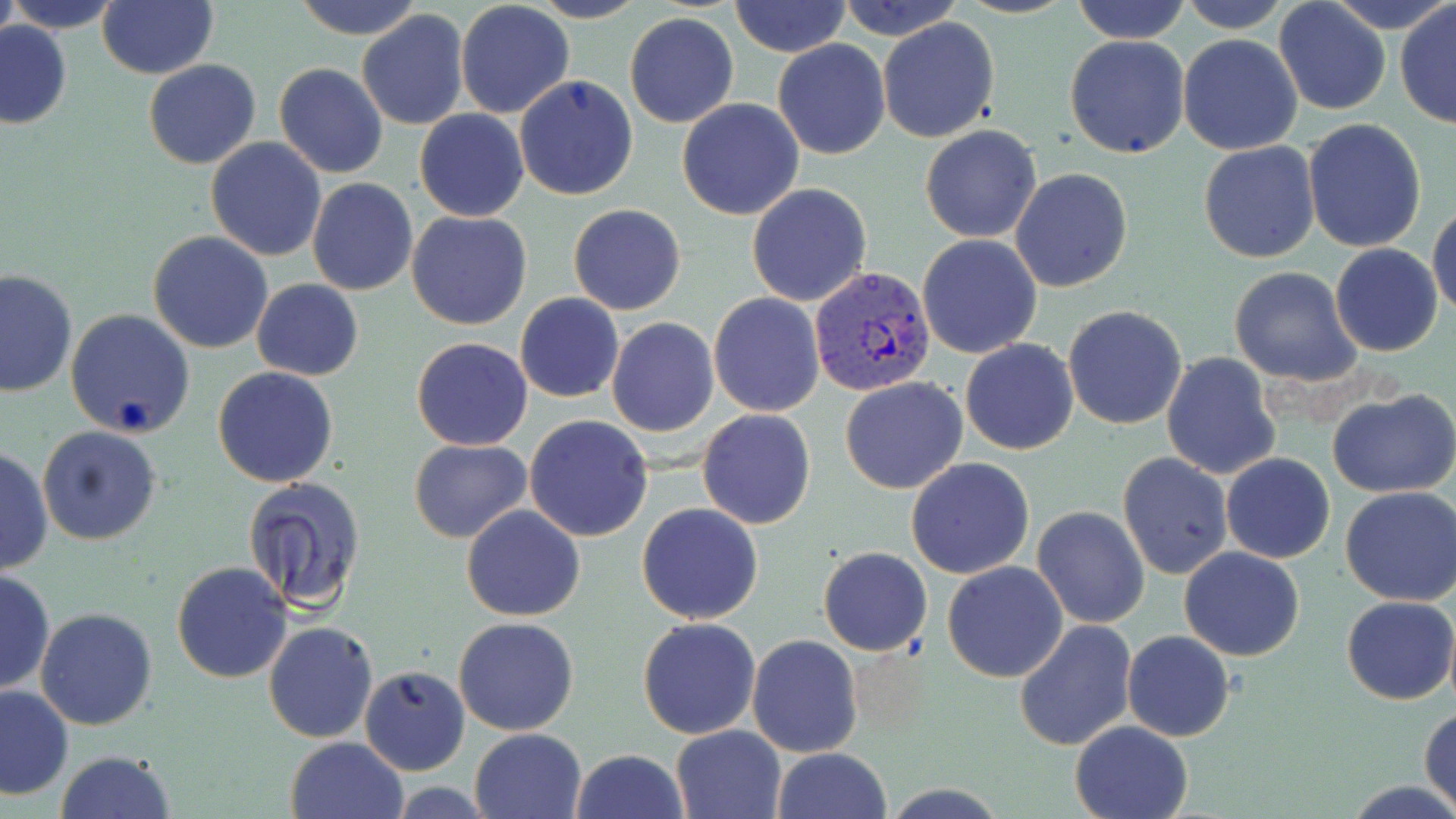
slide-level diagnosis = Plasmodium vivax
magnification = 1000x
modality = light microscopy
field of view = one of a larger specimen
preparation = thin blood smear
Plasmodium vivax-infected red blood cell locations = approximate bounding boxes as (x1,y1)-(x2,y2) corner pairs in pixels: (811,265)-(942,400)
uninfected red blood cell locations = approximate bounding boxes as (x1,y1)-(x2,y2) corner pairs in pixels: (1,0)-(19,55), (7,0)-(125,32), (96,0)-(217,79), (288,0)-(424,37), (528,0)-(647,23), (841,0)-(957,40), (1071,0)-(1191,43), (1179,0)-(1292,32), (1332,0)-(1450,29), (729,1)-(850,56), (1273,1)-(1390,116), (455,2)-(575,120), (1394,4)-(1455,129), (355,10)-(469,129), (624,12)-(739,129), (878,17)-(1000,143), (1,18)-(73,129), (1063,34)-(1191,159), (1177,34)-(1304,156), (773,38)-(891,159), (142,59)-(261,170), (275,63)-(388,179), (514,74)-(639,202), (677,98)-(805,221), (415,110)-(529,222), (1301,117)-(1429,253), (919,124)-(1043,243), (205,137)-(326,261), (1198,140)-(1323,264), (1011,167)-(1133,292), (307,179)-(417,295), (746,183)-(872,305), (568,203)-(687,315), (1428,203)-(1456,320), (407,211)-(531,330), (147,230)-(274,354), (916,234)-(1042,359), (1331,244)-(1443,358), (1230,267)-(1364,387), (0,268)-(78,398), (251,278)-(363,380), (708,292)-(825,417), (515,293)-(624,403), (1061,305)-(1188,430), (64,308)-(196,438), (607,318)-(719,438), (411,337)-(532,451), (961,338)-(1079,456), (1161,351)-(1284,480), (212,366)-(339,488), (839,376)-(969,495), (1328,389)-(1456,495), (697,409)-(817,529), (525,415)-(654,541), (38,426)-(163,547), (407,438)-(532,543), (1,445)-(52,579), (1118,453)-(1232,580), (1221,453)-(1335,564), (905,456)-(1035,579), (242,479)-(366,613), (1338,487)-(1456,606), (461,504)-(585,620), (637,504)-(765,624), (1031,506)-(1149,629), (818,547)-(932,656), (1179,548)-(1305,661), (942,560)-(1069,682), (171,561)-(292,684), (0,568)-(54,696), (1342,595)-(1455,704), (34,607)-(158,731), (453,617)-(580,736), (638,617)-(761,738), (1013,619)-(1138,751), (264,620)-(379,742), (1122,631)-(1235,742), (748,634)-(864,758), (360,664)-(468,774), (1,684)-(75,799), (1420,706)-(1456,815), (1069,719)-(1195,819), (669,724)-(787,819), (469,728)-(586,818), (286,737)-(409,819), (772,747)-(892,819), (572,748)-(687,819), (56,750)-(178,819), (1342,779)-(1456,818)
stain = May-Grünwald-Giemsa
image size = 1456×819 pixels